Outline each blood parasite and name the species.
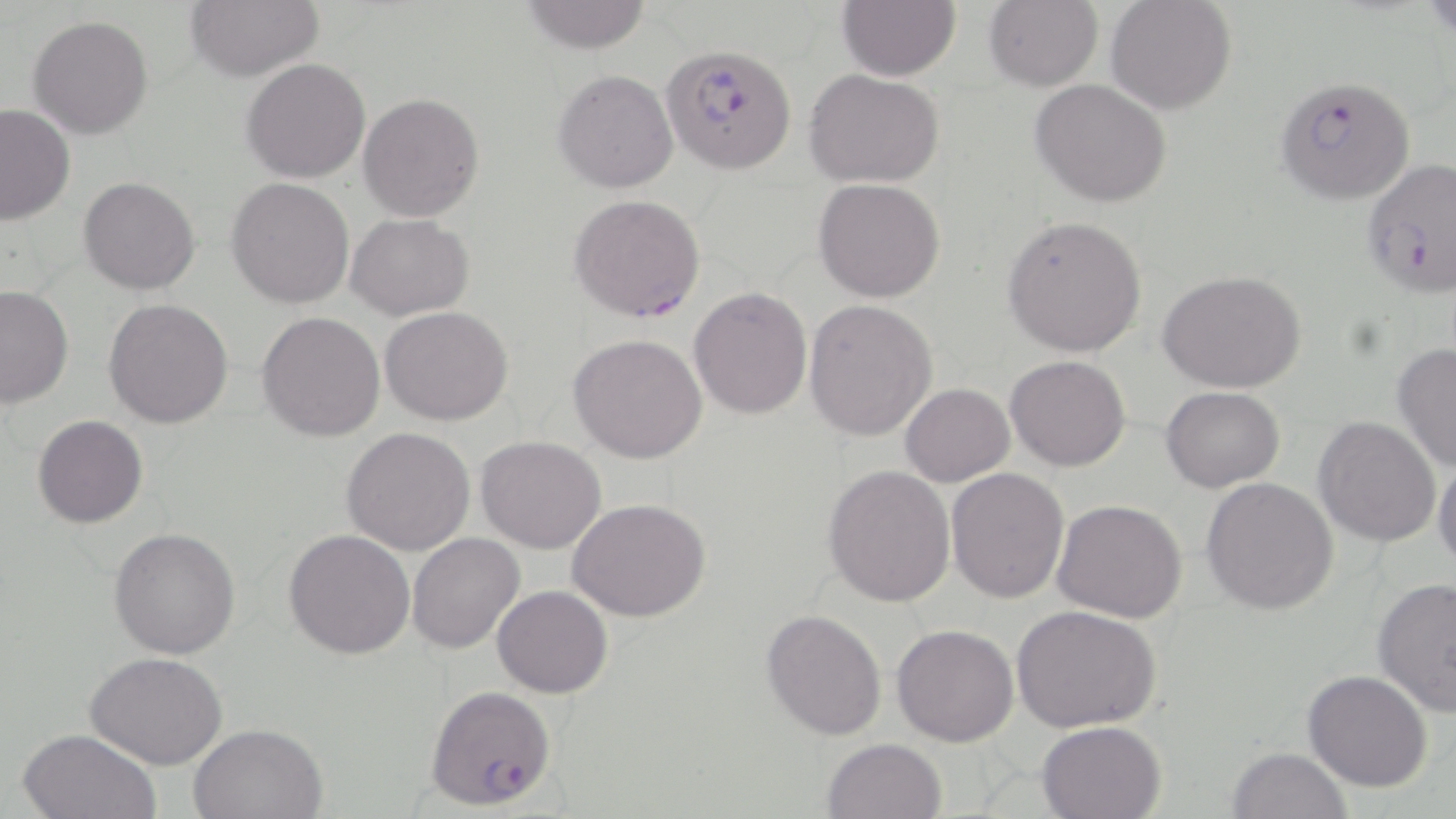

Approximate bounding boxes as named x1/y1/x2/y2 corners in pixels.
Plasmodium falciparum-infected red blood cells: (x1=663, y1=44, x2=796, y2=173), (x1=1274, y1=74, x2=1416, y2=205), (x1=1359, y1=157, x2=1456, y2=298), (x1=569, y1=193, x2=707, y2=322), (x1=428, y1=686, x2=555, y2=809).
No Plasmodium ovale, Plasmodium malariae, Plasmodium vivax, Babesia divergens, or Trypanosoma brucei observed.

Summary:
  - Uninfected red blood cell locations: (x1=184, y1=0, x2=325, y2=80), (x1=838, y1=0, x2=960, y2=81), (x1=1105, y1=0, x2=1238, y2=115), (x1=519, y1=1, x2=652, y2=53), (x1=982, y1=1, x2=1102, y2=90), (x1=28, y1=16, x2=155, y2=139), (x1=242, y1=58, x2=370, y2=183), (x1=804, y1=68, x2=947, y2=187), (x1=553, y1=69, x2=677, y2=193), (x1=1030, y1=78, x2=1172, y2=207), (x1=358, y1=93, x2=484, y2=220), (x1=0, y1=103, x2=77, y2=226), (x1=79, y1=176, x2=201, y2=295), (x1=814, y1=178, x2=946, y2=302), (x1=226, y1=179, x2=355, y2=308), (x1=346, y1=214, x2=475, y2=321), (x1=1002, y1=214, x2=1146, y2=356), (x1=1158, y1=271, x2=1306, y2=393), (x1=1, y1=285, x2=75, y2=408), (x1=689, y1=288, x2=812, y2=419), (x1=104, y1=297, x2=234, y2=429), (x1=804, y1=299, x2=938, y2=441), (x1=379, y1=306, x2=512, y2=425), (x1=257, y1=312, x2=385, y2=442), (x1=569, y1=333, x2=708, y2=463), (x1=1391, y1=342, x2=1456, y2=474), (x1=1005, y1=354, x2=1130, y2=472), (x1=900, y1=383, x2=1014, y2=485), (x1=1161, y1=385, x2=1286, y2=493), (x1=32, y1=414, x2=149, y2=528), (x1=1313, y1=415, x2=1441, y2=546), (x1=342, y1=427, x2=476, y2=555), (x1=475, y1=437, x2=606, y2=554), (x1=1432, y1=457, x2=1456, y2=571), (x1=823, y1=466, x2=955, y2=606), (x1=946, y1=468, x2=1069, y2=603), (x1=1201, y1=477, x2=1339, y2=615), (x1=569, y1=497, x2=712, y2=622), (x1=1051, y1=498, x2=1189, y2=623), (x1=108, y1=528, x2=241, y2=659), (x1=282, y1=528, x2=414, y2=659), (x1=407, y1=532, x2=526, y2=655), (x1=1372, y1=575, x2=1455, y2=714), (x1=492, y1=585, x2=614, y2=697), (x1=1010, y1=604, x2=1161, y2=735), (x1=761, y1=608, x2=888, y2=740), (x1=891, y1=624, x2=1019, y2=747), (x1=86, y1=652, x2=228, y2=769), (x1=1303, y1=669, x2=1434, y2=791), (x1=1036, y1=719, x2=1169, y2=819), (x1=190, y1=722, x2=331, y2=819), (x1=16, y1=728, x2=161, y2=818), (x1=821, y1=738, x2=948, y2=819), (x1=1227, y1=747, x2=1350, y2=819)
  - Slide-level diagnosis: Plasmodium falciparum
  - Field of view: single
  - Modality: optical microscopy
  - Magnification: 1000x
  - Preparation: thin blood smear
  - Stain: May-Grünwald-Giemsa
  - Image size: 1456×819 pixels